Assess this cell for malaria.
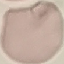
Uninfected.

Summary:
  - Preparation: thin smear
  - Stain: Giemsa
  - Capture: smartphone camera at the microscope eyepiece
  - Image type: automatically extracted cell patch, resized to 64 × 64 pixels